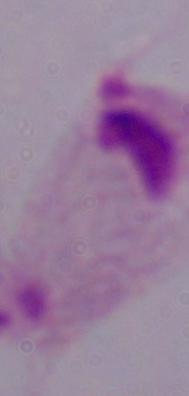

A trichomonad is seen. Captured at 1000x magnification. Photomicrograph.